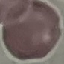
Result: negative for malaria parasites. Automatically extracted cell patch, resized to 64 × 64 pixels. Thin smear of blood. Giemsa stain. Photographed with a smartphone camera at the microscope eyepiece.